Report the malaria status of this cell.
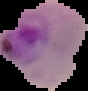
Parasitized.

Summary:
  - Image size: 88×91 pixels
  - Image type: segmented cell region with the area outside set to black
  - Preparation: thin blood smear